Name the parasite shown.
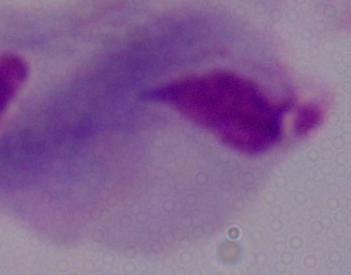
This is a trichomonad.

magnification = 1000x
modality = photomicrograph